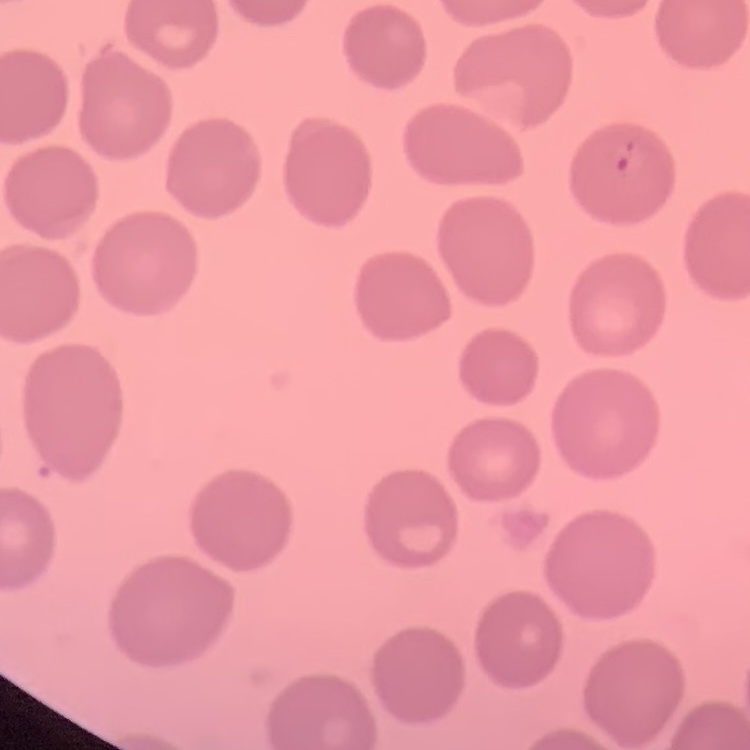
{
  "red_blood_cell_morphology": "no rouleaux formation",
  "image_type": "one tile cut from a larger photomicrograph",
  "preparation": "thin blood smear",
  "stain": "Field's or Giemsa"
}